Outline each uninfected red blood cell.
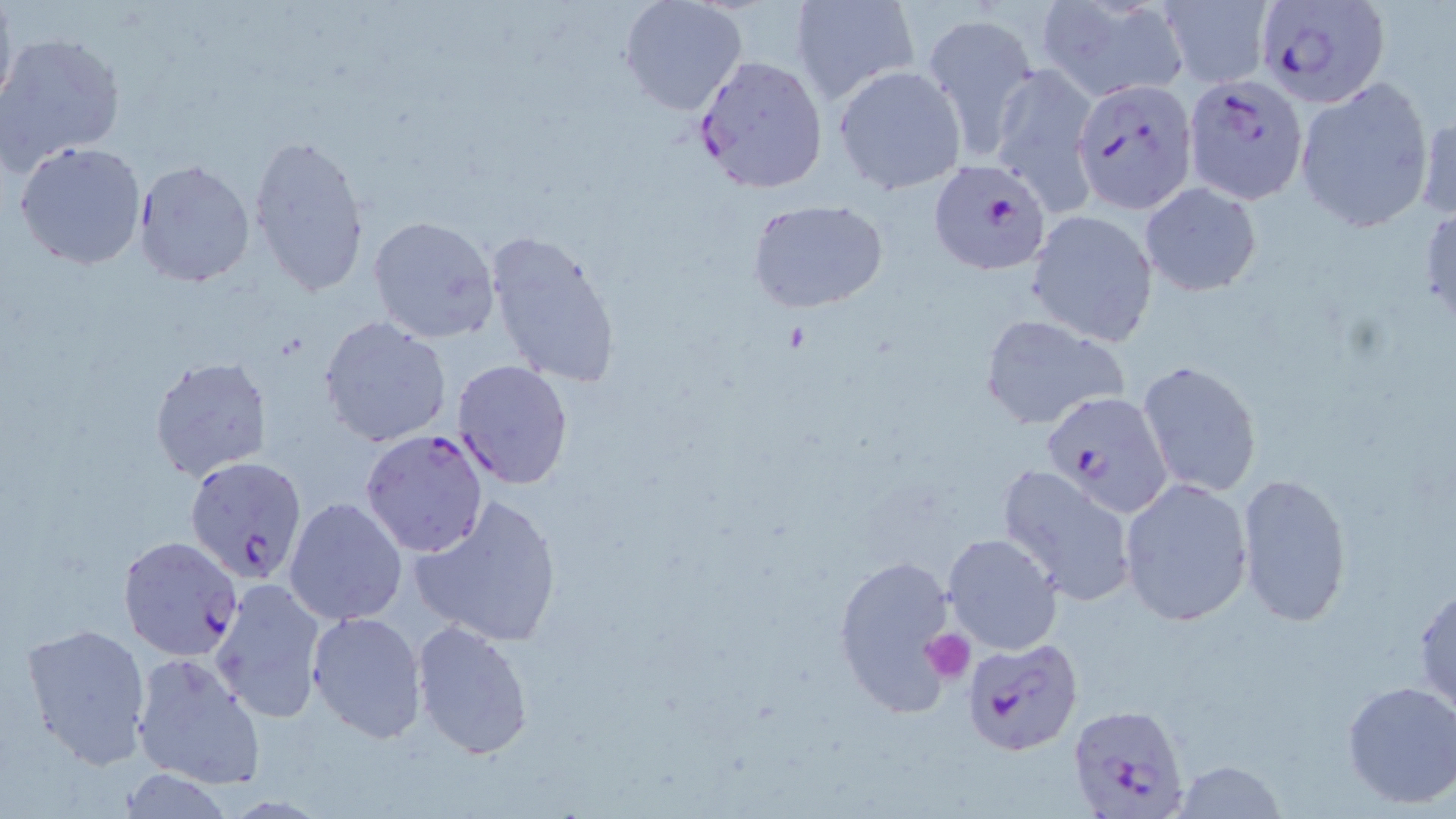

Approximate bounding boxes as (x1, y1, x2, y2) in pixels.
Uninfected red blood cells: (0, 0, 17, 116), (617, 0, 747, 115), (790, 0, 920, 106), (1038, 0, 1187, 101), (1158, 1, 1273, 87), (920, 9, 1041, 159), (0, 32, 125, 174), (990, 62, 1097, 214), (833, 65, 966, 194), (1297, 79, 1435, 229), (1415, 110, 1456, 226), (248, 136, 372, 299), (14, 141, 147, 269), (133, 159, 255, 286), (1138, 182, 1262, 298), (1419, 198, 1455, 332), (749, 200, 889, 315), (1026, 210, 1159, 346), (366, 214, 500, 343), (483, 227, 624, 391), (977, 312, 1131, 432), (319, 315, 452, 448), (148, 355, 272, 480), (1136, 358, 1263, 499), (452, 359, 574, 489), (996, 464, 1138, 607), (1236, 472, 1355, 628), (1120, 477, 1254, 627), (409, 495, 563, 647), (284, 496, 408, 626), (941, 531, 1063, 655), (832, 550, 961, 718), (210, 577, 329, 723), (1412, 582, 1456, 714), (306, 610, 426, 744), (410, 619, 534, 763), (20, 623, 152, 768), (131, 650, 266, 790), (1340, 678, 1456, 810), (1171, 761, 1290, 817).

Summary:
  - Plasmodium falciparum-infected red blood cell locations: (1260, 1, 1389, 109), (691, 54, 829, 194), (1185, 75, 1309, 203), (1074, 78, 1199, 212), (929, 158, 1052, 274), (1042, 392, 1172, 518), (360, 428, 489, 558), (185, 458, 309, 584), (116, 534, 245, 662), (960, 635, 1085, 755), (1066, 702, 1191, 818)
  - Platelet locations: (923, 631, 973, 681)
  - Slide-level diagnosis: Plasmodium falciparum
  - Magnification: 1000x
  - Stain: May-Grünwald-Giemsa
  - Image size: 1456×819 pixels
  - Preparation: thin blood film
  - Field of view: one of a larger specimen
  - Modality: light microscopy